State the blood parasite species.
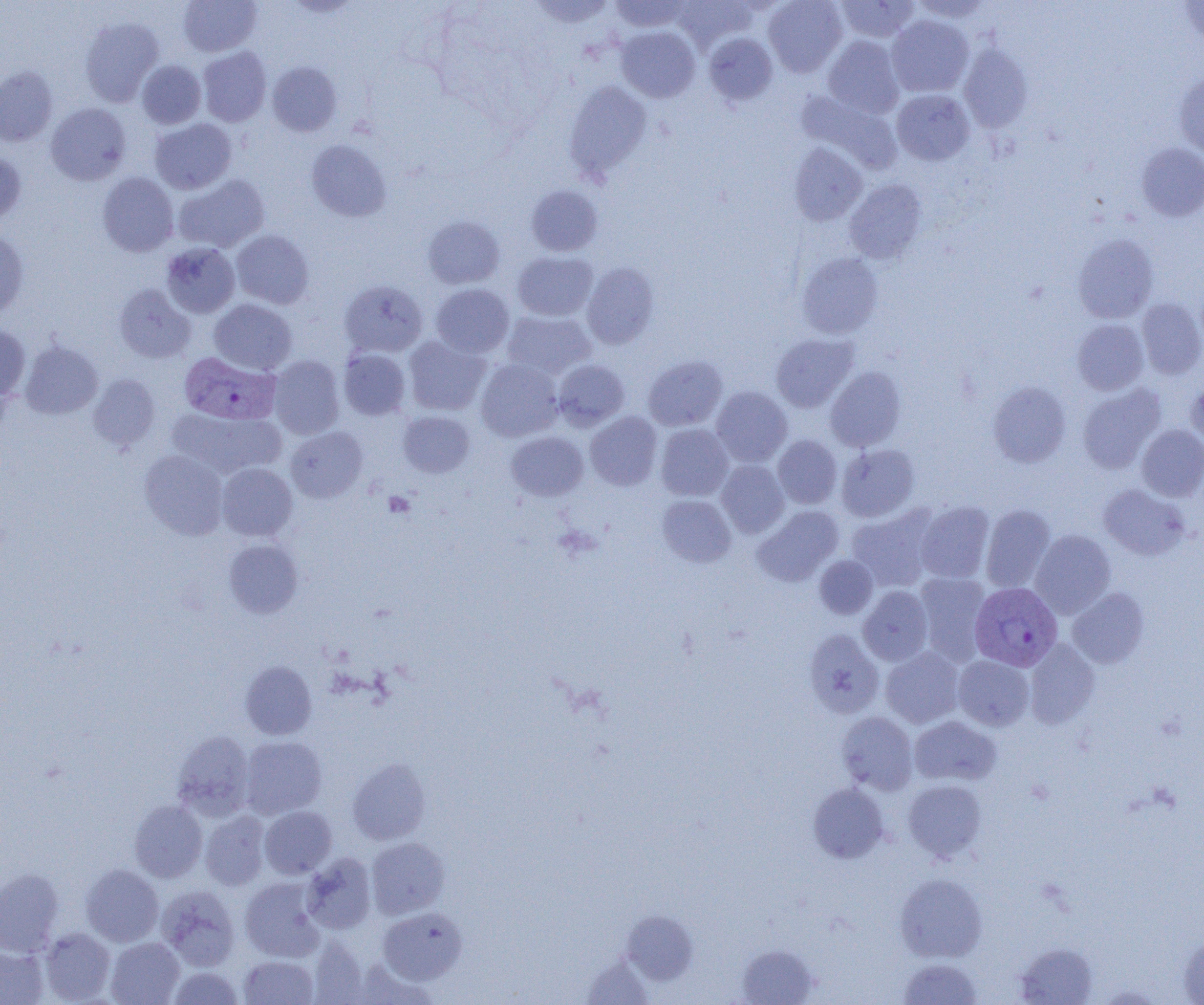

Plasmodium vivax.

Summary:
  - Coordinate format: approximate bounding boxes as named x1/y1/x2/y2 corners in pixels
  - Uninfected red blood cell locations: (x1=178, y1=0, x2=261, y2=56), (x1=528, y1=0, x2=616, y2=27), (x1=609, y1=0, x2=692, y2=32), (x1=672, y1=0, x2=755, y2=52), (x1=764, y1=0, x2=847, y2=77), (x1=834, y1=0, x2=919, y2=43), (x1=910, y1=0, x2=993, y2=23), (x1=1180, y1=0, x2=1204, y2=44), (x1=887, y1=15, x2=973, y2=97), (x1=79, y1=17, x2=164, y2=107), (x1=617, y1=26, x2=699, y2=103), (x1=703, y1=33, x2=777, y2=106), (x1=823, y1=36, x2=904, y2=118), (x1=958, y1=44, x2=1032, y2=132), (x1=198, y1=47, x2=271, y2=127), (x1=137, y1=60, x2=206, y2=129), (x1=267, y1=61, x2=342, y2=136), (x1=0, y1=66, x2=57, y2=147), (x1=1174, y1=72, x2=1204, y2=159), (x1=564, y1=80, x2=652, y2=181), (x1=891, y1=89, x2=974, y2=165), (x1=796, y1=90, x2=902, y2=174), (x1=46, y1=103, x2=131, y2=185), (x1=150, y1=118, x2=237, y2=194), (x1=306, y1=139, x2=392, y2=222), (x1=789, y1=143, x2=868, y2=226), (x1=1137, y1=143, x2=1204, y2=221), (x1=0, y1=150, x2=26, y2=226), (x1=98, y1=172, x2=179, y2=257), (x1=174, y1=174, x2=270, y2=253), (x1=845, y1=179, x2=927, y2=264), (x1=526, y1=185, x2=603, y2=256), (x1=423, y1=216, x2=504, y2=289), (x1=231, y1=230, x2=314, y2=309), (x1=0, y1=231, x2=29, y2=318), (x1=1073, y1=234, x2=1158, y2=323), (x1=161, y1=242, x2=240, y2=318), (x1=512, y1=251, x2=598, y2=321), (x1=797, y1=252, x2=883, y2=339), (x1=582, y1=263, x2=659, y2=349), (x1=340, y1=280, x2=427, y2=358), (x1=114, y1=283, x2=196, y2=363), (x1=431, y1=284, x2=514, y2=357), (x1=1137, y1=298, x2=1204, y2=379), (x1=210, y1=299, x2=297, y2=374), (x1=502, y1=310, x2=596, y2=380), (x1=1073, y1=319, x2=1149, y2=395), (x1=0, y1=324, x2=30, y2=402), (x1=771, y1=333, x2=858, y2=412), (x1=404, y1=335, x2=491, y2=415), (x1=20, y1=342, x2=102, y2=419), (x1=338, y1=349, x2=411, y2=420), (x1=268, y1=355, x2=345, y2=439), (x1=644, y1=355, x2=727, y2=430), (x1=476, y1=359, x2=563, y2=441), (x1=553, y1=359, x2=629, y2=430), (x1=826, y1=366, x2=906, y2=451), (x1=88, y1=374, x2=160, y2=450), (x1=1186, y1=377, x2=1204, y2=447), (x1=988, y1=381, x2=1071, y2=467), (x1=1078, y1=384, x2=1165, y2=474), (x1=711, y1=387, x2=792, y2=466), (x1=166, y1=408, x2=285, y2=479), (x1=398, y1=410, x2=475, y2=478), (x1=586, y1=411, x2=662, y2=490), (x1=656, y1=424, x2=733, y2=501), (x1=1137, y1=424, x2=1204, y2=501), (x1=286, y1=427, x2=367, y2=502), (x1=506, y1=431, x2=588, y2=501), (x1=772, y1=435, x2=842, y2=508), (x1=837, y1=444, x2=919, y2=522), (x1=140, y1=450, x2=228, y2=539), (x1=716, y1=460, x2=789, y2=537), (x1=217, y1=463, x2=297, y2=541), (x1=1099, y1=484, x2=1190, y2=560), (x1=657, y1=495, x2=735, y2=567), (x1=915, y1=501, x2=994, y2=583), (x1=980, y1=504, x2=1055, y2=592), (x1=753, y1=506, x2=843, y2=586), (x1=846, y1=507, x2=938, y2=592), (x1=1030, y1=530, x2=1116, y2=618), (x1=225, y1=539, x2=303, y2=617), (x1=814, y1=555, x2=878, y2=619), (x1=914, y1=573, x2=991, y2=664), (x1=859, y1=586, x2=933, y2=665), (x1=1067, y1=587, x2=1149, y2=668), (x1=803, y1=629, x2=884, y2=718), (x1=1024, y1=639, x2=1100, y2=729), (x1=881, y1=647, x2=964, y2=728), (x1=953, y1=655, x2=1033, y2=730), (x1=241, y1=661, x2=316, y2=739), (x1=837, y1=711, x2=918, y2=794), (x1=909, y1=716, x2=1001, y2=787), (x1=172, y1=730, x2=256, y2=820), (x1=239, y1=736, x2=327, y2=819), (x1=347, y1=758, x2=430, y2=845), (x1=903, y1=779, x2=987, y2=862), (x1=808, y1=782, x2=889, y2=863), (x1=129, y1=800, x2=207, y2=882), (x1=260, y1=806, x2=336, y2=878), (x1=201, y1=811, x2=270, y2=891), (x1=366, y1=837, x2=449, y2=918), (x1=302, y1=852, x2=376, y2=934), (x1=81, y1=864, x2=164, y2=946), (x1=0, y1=868, x2=63, y2=956), (x1=895, y1=874, x2=987, y2=962), (x1=240, y1=877, x2=325, y2=961), (x1=157, y1=885, x2=240, y2=971), (x1=378, y1=907, x2=467, y2=984), (x1=621, y1=910, x2=698, y2=984), (x1=40, y1=928, x2=116, y2=1003), (x1=1179, y1=935, x2=1204, y2=1004), (x1=309, y1=937, x2=369, y2=1004), (x1=106, y1=938, x2=184, y2=1005), (x1=1015, y1=942, x2=1098, y2=1004), (x1=737, y1=944, x2=818, y2=1004), (x1=0, y1=945, x2=48, y2=1004), (x1=239, y1=955, x2=318, y2=1004), (x1=581, y1=957, x2=654, y2=1004), (x1=898, y1=957, x2=983, y2=1004), (x1=168, y1=967, x2=243, y2=1004)
  - Platelet locations: (x1=383, y1=492, x2=415, y2=517)
  - Plasmodium vivax-infected red blood cell locations: (x1=179, y1=352, x2=281, y2=425), (x1=970, y1=582, x2=1063, y2=670)
  - Preparation: thin blood smear
  - Modality: light microscopy
  - Magnification: 1000x
  - Image size: 1204×1005 pixels
  - Field of view: one of a larger specimen